Classify this cell by malaria status.
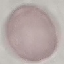
It is uninfected.

Summary:
  - Capture: smartphone camera at the microscope eyepiece
  - Image type: cell patch, automatically extracted from a larger field of view and resized to 64 × 64 pixels
  - Stain: Giemsa
  - Preparation: thin blood smear